Identify the parasite.
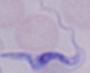
A trypanosome.

Micrograph. Captured at 1000x magnification.